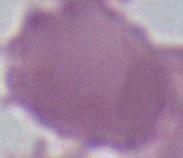
Summary:
  - Magnification: 1000x
  - Identification: erythrocyte
  - Modality: photomicrograph